Classify this cell by malaria status.
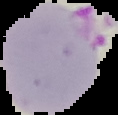
It is parasitized.

preparation = thin blood smear
image type = segmented cell region with the area outside set to black
image size = 118×115 pixels